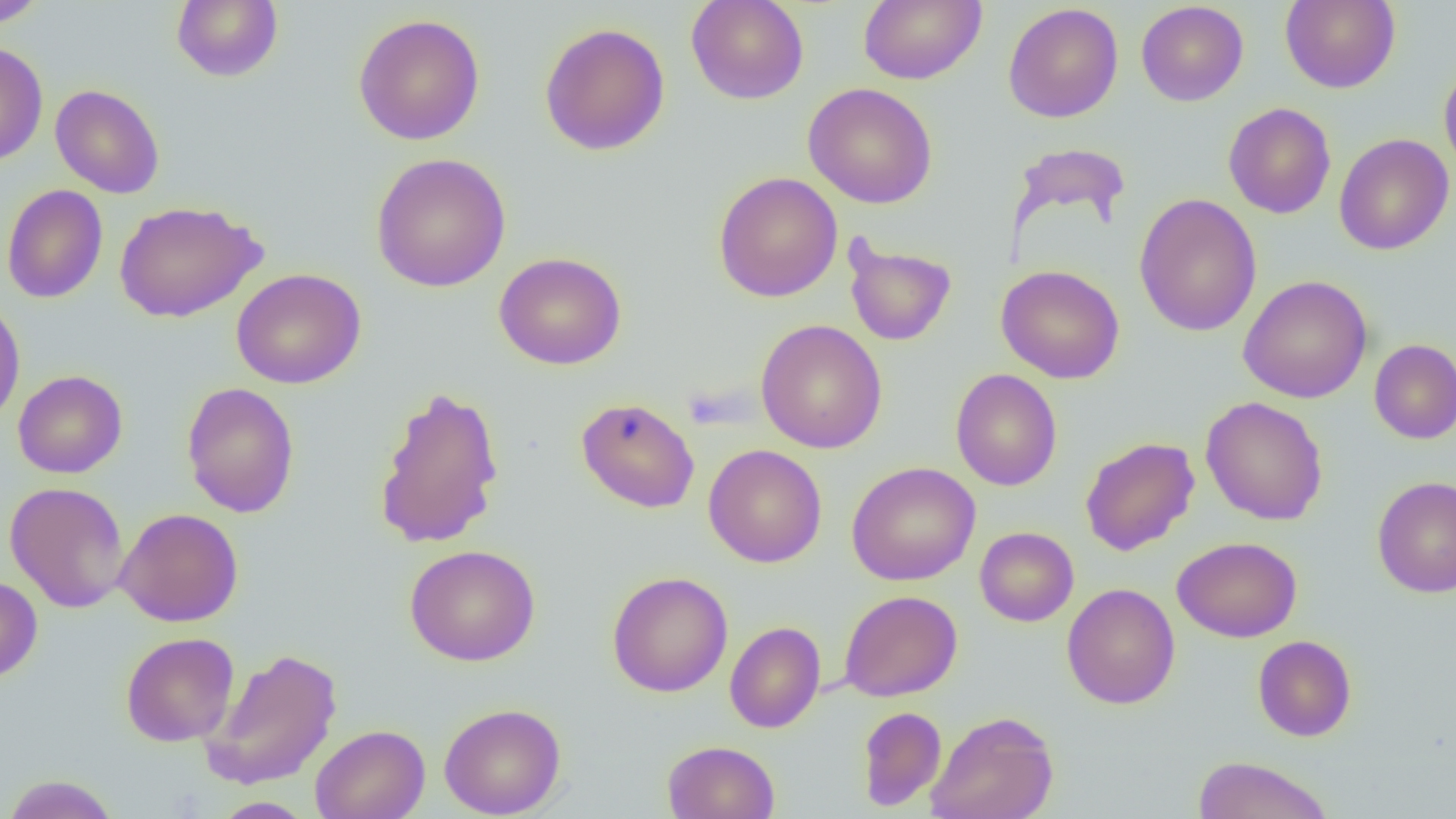
Summary:
  - Coordinate format: approximate bounding boxes as (x1,y1)-(x2,y2) corner pairs in pixels
  - Uninfected red blood cell locations: (1,0)-(48,28), (171,0)-(284,83), (686,0)-(809,105), (858,0)-(987,85), (1280,0)-(1400,93), (1136,1)-(1249,106), (1003,3)-(1123,123), (353,13)-(486,146), (539,22)-(670,156), (0,41)-(49,166), (1439,62)-(1456,180), (803,83)-(938,209), (50,84)-(165,198), (1223,102)-(1336,219), (1334,133)-(1454,255), (1008,142)-(1131,238), (370,153)-(511,293), (713,171)-(843,302), (1,184)-(108,304), (1134,193)-(1262,337), (114,200)-(266,323), (843,237)-(957,346), (494,252)-(627,370), (996,265)-(1125,384), (231,268)-(366,389), (1238,274)-(1374,404), (0,297)-(26,428), (756,319)-(887,453), (1369,339)-(1456,444), (951,368)-(1062,491), (13,370)-(127,478), (181,382)-(300,518), (373,386)-(505,550), (1201,396)-(1328,525), (576,397)-(700,513), (1080,436)-(1200,556), (703,444)-(827,568), (846,461)-(980,585), (1371,476)-(1455,598), (5,481)-(130,613), (115,507)-(244,627), (975,526)-(1079,626), (1172,536)-(1302,642), (404,544)-(541,666), (607,571)-(733,697), (0,575)-(42,684), (1062,583)-(1180,709), (839,590)-(962,701), (725,621)-(825,733), (121,631)-(239,747), (1253,635)-(1357,741), (199,648)-(342,791), (439,702)-(567,818), (857,706)-(946,811), (926,710)-(1058,819), (310,724)-(430,819), (662,740)-(780,819), (1191,755)-(1336,819), (1,774)-(121,819), (211,797)-(316,818)
  - Slide-level diagnosis: negative for blood parasites
  - Field of view: single
  - Preparation: thin blood film
  - Modality: optical microscopy
  - Magnification: 1000x
  - Image size: 1456×819 pixels